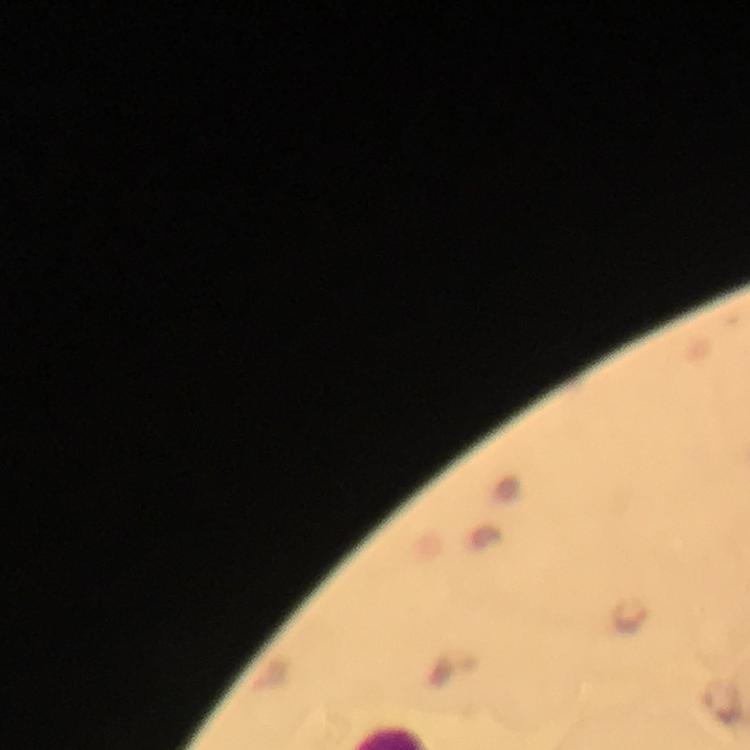
malaria parasite locations = approximate centers as [x, y] in pixels: [630, 615]
context = from a diagnostic examination for malaria
image size = 750×750 pixels
stain = Giemsa
magnification = 100x
immersion oil = used
preparation = thick blood film
capture = smartphone camera through the microscope
cropped from = a single field of view